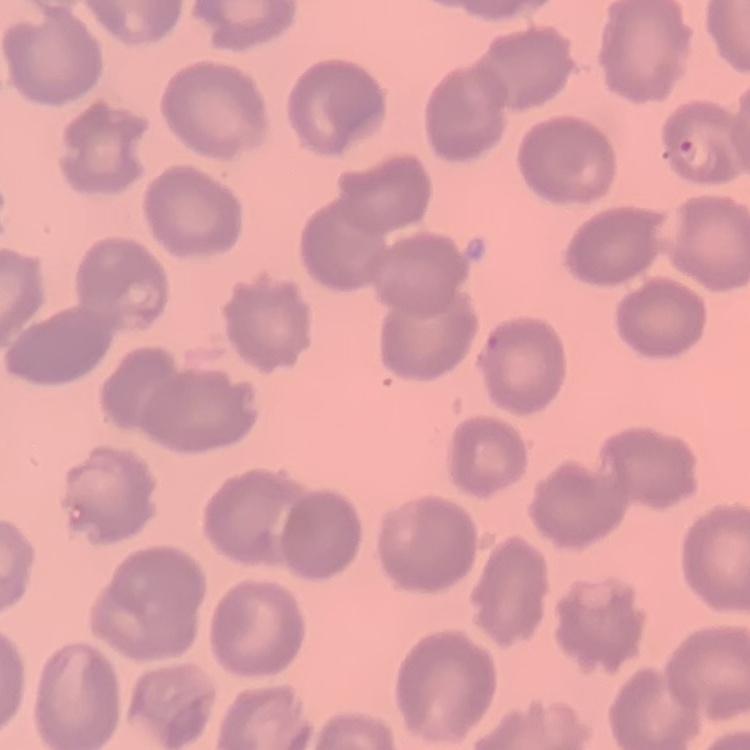

Summary:
  - Erythrocyte morphology: no rouleaux formation
  - Preparation: thin blood smear
  - Image type: one tile cut from a larger photomicrograph
  - Stain: Field's or Giemsa